Outline each blood parasite and name the species.
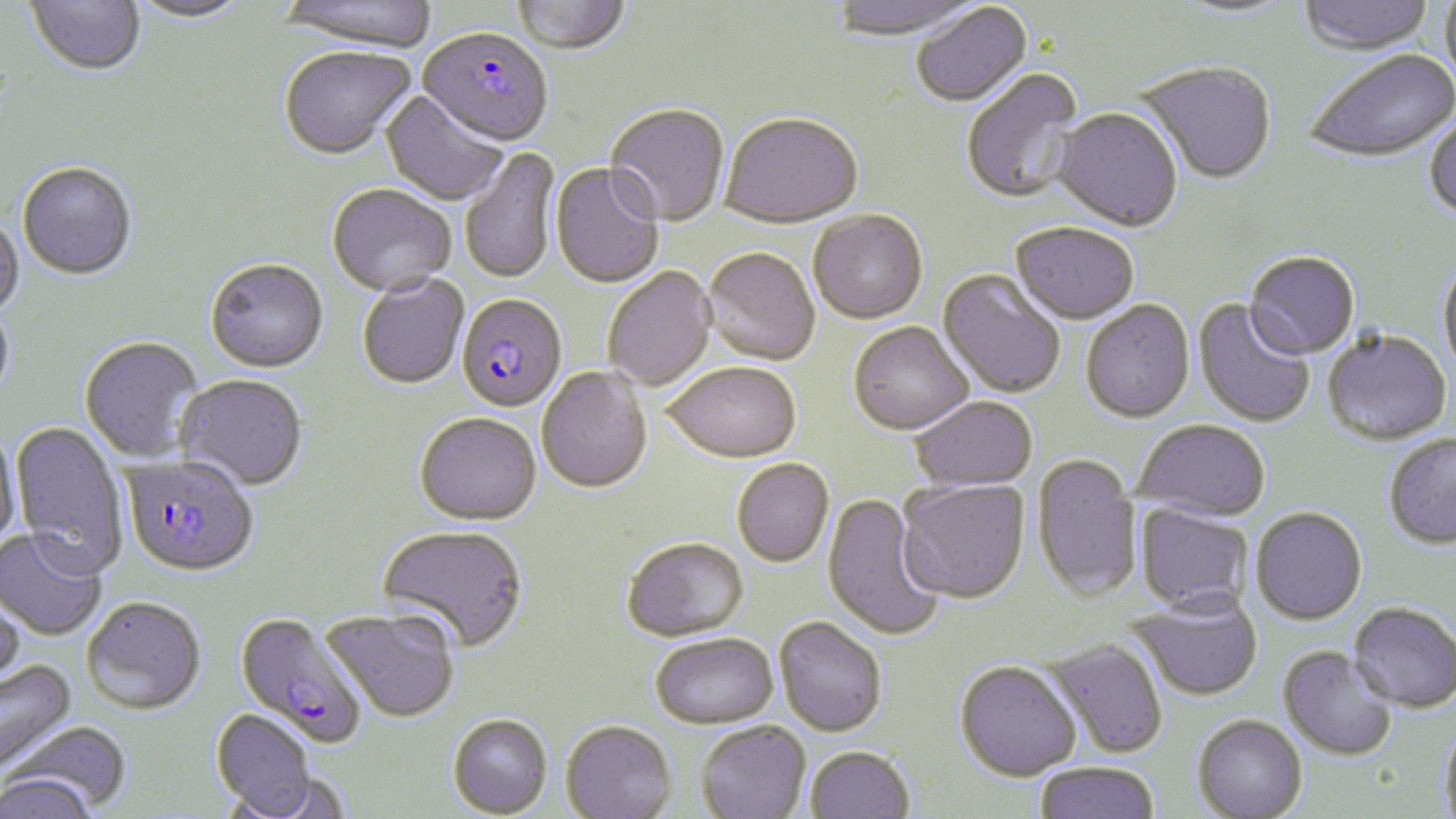

Approximate bounding boxes as (x1, y1, x2, y2) in pixels.
Plasmodium falciparum-infected red blood cells: (418, 30, 552, 149), (457, 296, 567, 414), (121, 456, 258, 579), (234, 613, 368, 749).
No Plasmodium ovale, Plasmodium malariae, Plasmodium vivax, Babesia divergens, or Trypanosoma brucei observed.

{
  "slide_level_diagnosis": "Plasmodium falciparum",
  "image_size": "1456×819 pixels",
  "stain": "May-Grünwald-Giemsa",
  "modality": "light microscopy",
  "uninfected_red_blood_cell_locations": "approximate bounding boxes as (x1, y1, x2, y2) in pixels: (25, 0, 146, 79), (127, 0, 253, 26), (279, 0, 437, 56), (829, 0, 984, 43), (1298, 0, 1436, 56), (512, 1, 631, 56), (1172, 1, 1297, 22), (1439, 1, 1456, 90), (911, 4, 1033, 109), (279, 48, 417, 162), (1302, 50, 1455, 165), (1136, 63, 1277, 186), (961, 69, 1086, 206), (380, 91, 509, 207), (605, 105, 730, 229), (1052, 109, 1183, 234), (1424, 111, 1456, 223), (720, 116, 863, 231), (460, 146, 561, 286), (17, 164, 137, 282), (550, 164, 664, 290), (327, 186, 456, 299), (808, 213, 928, 326), (0, 214, 25, 320), (1010, 222, 1139, 325), (702, 250, 820, 367), (1244, 251, 1360, 360), (1437, 258, 1456, 381), (205, 261, 329, 375), (603, 268, 718, 392), (937, 270, 1066, 399), (357, 275, 470, 391), (1081, 300, 1195, 423), (1194, 300, 1315, 428), (0, 301, 16, 406), (848, 323, 975, 436), (1322, 329, 1452, 445), (79, 337, 204, 464), (664, 363, 801, 464), (536, 368, 653, 495), (174, 376, 308, 492), (909, 397, 1038, 491), (414, 415, 541, 528), (1133, 419, 1270, 520), (10, 421, 130, 577), (0, 427, 21, 551), (1383, 433, 1456, 548), (1032, 453, 1142, 601), (732, 459, 834, 567), (896, 477, 1030, 604), (822, 493, 945, 642), (1135, 502, 1255, 612), (1250, 506, 1368, 624), (376, 526, 529, 655), (0, 529, 108, 642), (622, 537, 749, 643), (0, 592, 26, 696), (1128, 593, 1263, 701), (81, 597, 206, 716), (1348, 601, 1455, 713), (321, 609, 460, 724), (774, 616, 887, 737), (651, 633, 778, 728), (1043, 638, 1169, 759), (1279, 645, 1398, 761), (954, 659, 1081, 780), (0, 661, 78, 777), (211, 710, 320, 818), (447, 714, 554, 818), (1192, 714, 1308, 818), (1439, 717, 1456, 818), (7, 719, 134, 815), (560, 719, 677, 819), (695, 721, 811, 819), (805, 745, 916, 818), (1033, 761, 1160, 819), (2, 773, 99, 819)",
  "magnification": "1000x",
  "preparation": "thin blood smear",
  "field_of_view": "one of a larger specimen"
}